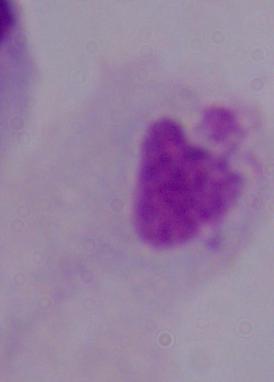 A trichomonad is shown. 1000x magnification. Micrograph.